Report the malaria status of this cell.
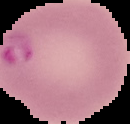
Parasitized.

Image is 130×124 pixels. Cell region segmented out of the field of view; the surrounding area is masked to black. From a thin blood film.